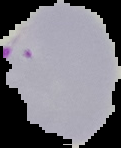

preparation = thin blood smear
image type = cell region segmented out of the field of view; surrounding area masked to black
result = malaria parasites identified
image size = 121×148 pixels